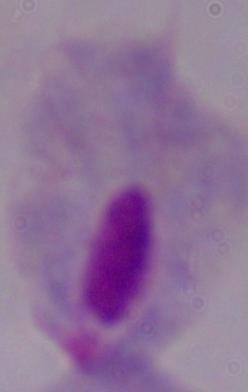

Summary:
  - Magnification: 1000x
  - Identification: trichomonad
  - Modality: photomicrograph